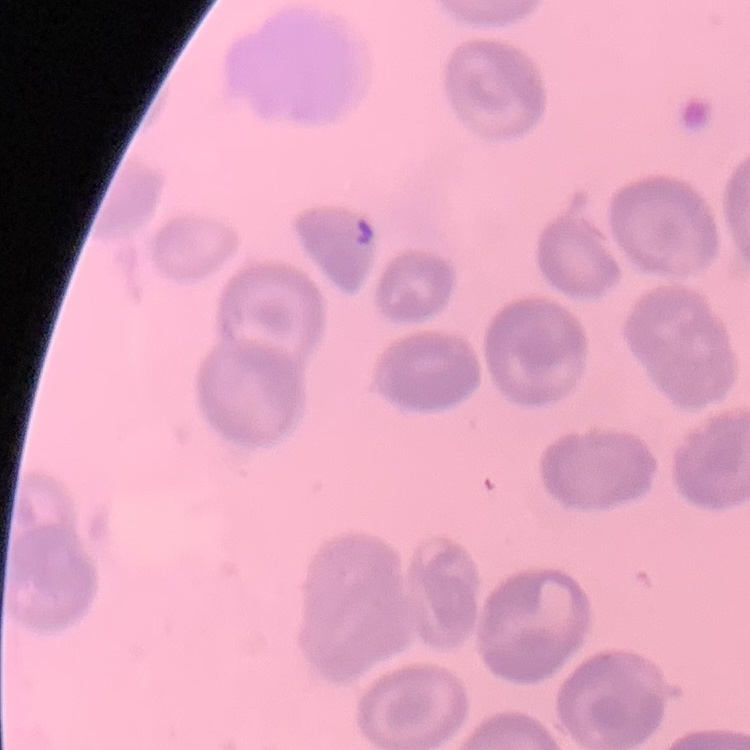

Summary:
  - Red blood cell morphology: no rouleaux formation
  - Stain: Field's or Giemsa
  - Preparation: thin blood film
  - Image type: one tile cut from a larger photomicrograph